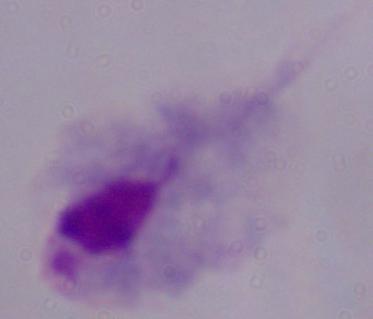

{
  "modality": "photomicrograph",
  "magnification": "1000x",
  "identification": "trichomonad"
}